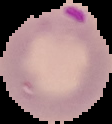
Image is 112×124 pixels. The area outside the segmented cell region is set to black. Malaria status: parasitized. From a thin blood film.